Assess this cell for malaria.
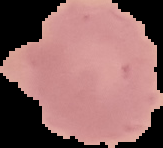

It is uninfected.

image size = 163×148 pixels
image type = segmented cell region on a black background
preparation = thin blood film